State which cell type is depicted.
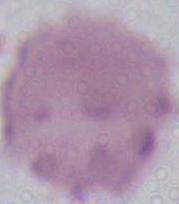

This is an erythrocyte.

1000x magnification. Photomicrograph.